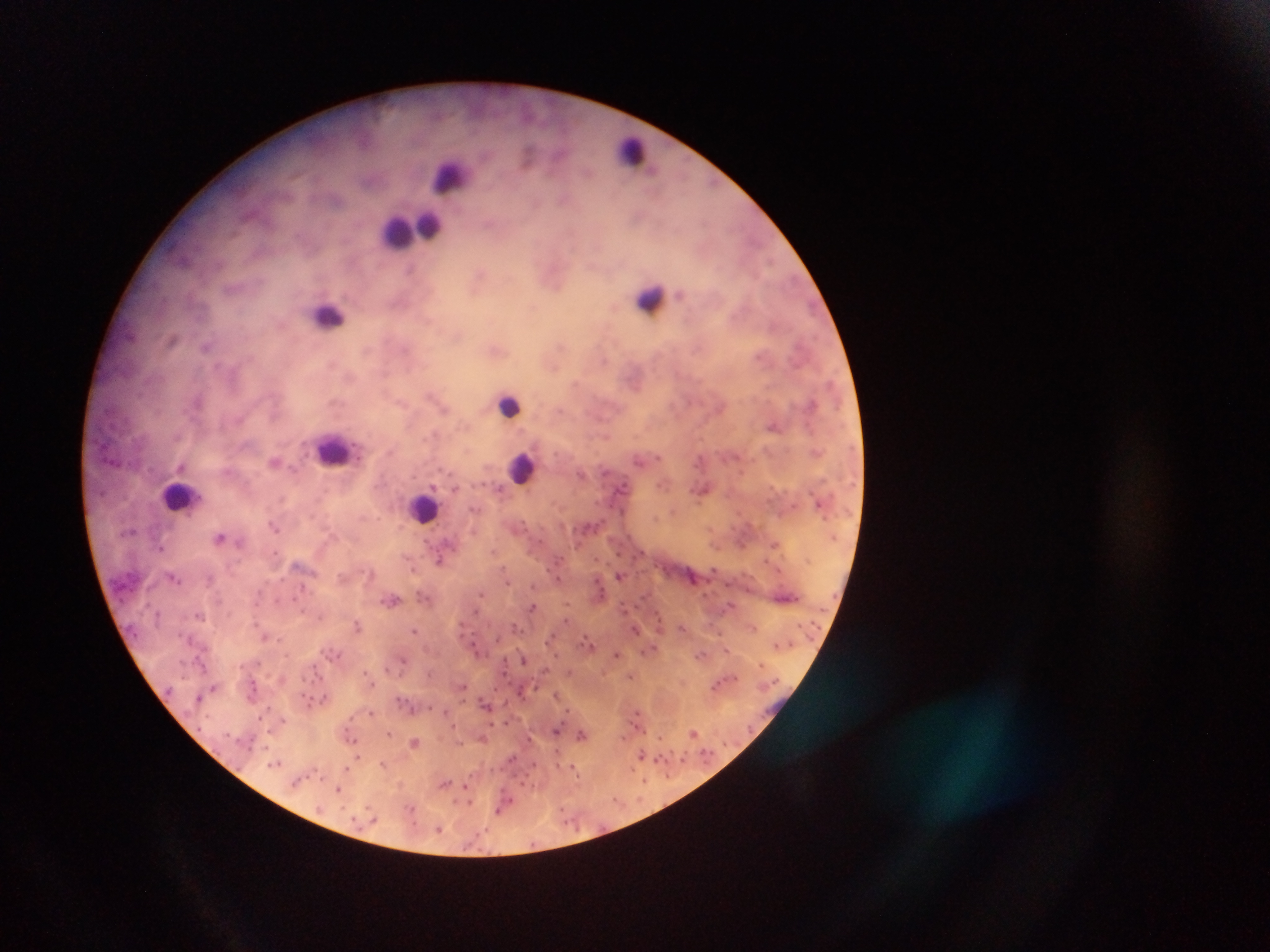

{
  "capture": "mobile-phone photograph through a microscope",
  "leukocyte_locations": "approximate centers as [x, y] in pixels: [632, 152], [450, 179], [408, 229], [652, 300], [328, 315], [510, 406], [334, 449], [521, 469], [181, 496], [424, 507]",
  "image_size": "1270×952 pixels",
  "field_of_view": "single",
  "country": "Ghana",
  "malaria_parasite_locations": "approximate centers as [x, y] in pixels (subset; some below the resolvable size): [529, 156], [718, 182], [207, 345], [774, 426], [855, 448], [658, 458], [736, 458], [276, 462], [725, 462], [639, 466], [744, 472], [607, 473], [481, 482], [856, 483], [493, 484], [660, 484], [624, 485], [472, 486], [456, 487], [703, 489], [813, 493], [820, 503], [793, 506], [612, 507], [468, 509], [624, 510], [673, 510], [825, 519], [522, 521], [275, 525], [747, 525], [577, 529], [595, 529], [134, 532], [834, 536], [220, 537], [530, 537], [542, 543], [775, 544], [719, 546], [162, 548], [495, 551], [274, 553], [619, 553], [644, 553], [564, 557], [633, 558], [598, 559], [807, 559], [440, 560], [763, 560], [503, 567], [413, 570], [716, 570], [548, 571], [778, 572], [620, 575], [174, 577], [282, 579], [595, 580], [558, 581], [267, 582], [507, 583], [302, 584], [532, 584], [727, 584], [603, 588], [746, 590], [262, 591], [418, 593], [481, 593], [427, 596], [835, 596], [297, 597], [602, 597], [796, 598], [392, 600], [257, 602], [571, 603], [150, 606], [730, 606], [533, 607], [624, 607], [823, 609], [304, 610], [232, 612], [477, 612], [158, 615], [200, 615], [256, 617], [320, 617], [660, 621], [569, 622], [803, 622], [514, 625], [358, 626], [820, 627], [415, 629], [635, 630], [752, 630], [521, 632], [685, 632], [138, 635], [180, 635], [723, 635], [555, 636], [265, 637], [585, 638], [282, 639], [496, 640], [475, 645], [778, 645], [546, 646], [593, 646], [791, 646], [205, 647], [654, 647], [728, 649], [322, 650], [339, 653], [617, 653], [556, 654], [702, 654], [289, 656], [327, 658], [197, 659], [181, 660], [504, 660], [523, 660], [402, 661], [258, 663], [314, 663], [760, 663], [241, 667], [386, 668], [547, 671], [431, 673], [367, 674], [507, 674], [320, 676], [631, 676], [304, 679], [737, 679], [312, 681], [254, 682], [511, 682], [774, 683], [373, 685], [464, 685], [716, 685], [168, 689], [213, 689], [537, 689], [496, 690], [520, 690], [559, 694], [304, 695], [197, 697], [408, 697], [397, 698], [321, 700], [311, 701], [485, 703], [506, 703], [269, 708], [412, 708], [430, 708], [371, 711], [568, 711], [445, 712], [636, 714], [207, 717], [350, 717], [259, 718], [282, 720], [509, 722], [628, 723], [493, 724], [453, 726], [198, 728], [270, 729], [347, 730], [558, 730], [751, 730], [644, 732], [388, 733], [694, 733], [582, 734], [660, 735], [352, 738], [483, 738], [250, 739], [530, 740], [415, 742], [724, 743], [557, 749], [683, 752], [713, 752], [704, 753], [641, 755], [359, 757], [510, 760], [668, 760], [354, 761], [657, 761], [681, 761], [384, 763], [277, 764], [535, 764], [346, 766], [559, 767], [575, 770], [318, 771], [633, 772], [307, 775], [324, 775], [529, 777], [668, 778], [445, 782], [645, 783], [293, 784], [522, 784], [466, 787], [338, 790], [456, 800], [616, 801], [472, 803], [641, 803], [342, 807], [367, 807], [414, 807], [500, 809], [563, 809], [355, 819], [372, 821], [413, 823], [564, 823], [360, 829], [486, 829], [577, 829], [442, 830], [532, 845]",
  "preparation": "thick blood smear"
}